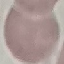

Summary:
  - Malaria status: uninfected
  - Preparation: thin smear
  - Capture: smartphone camera at the microscope eyepiece
  - Stain: Giemsa
  - Image type: cell patch, automatically extracted from a larger field of view and resized to 64 × 64 pixels